Give the position of every Plasmodium parasite visible.
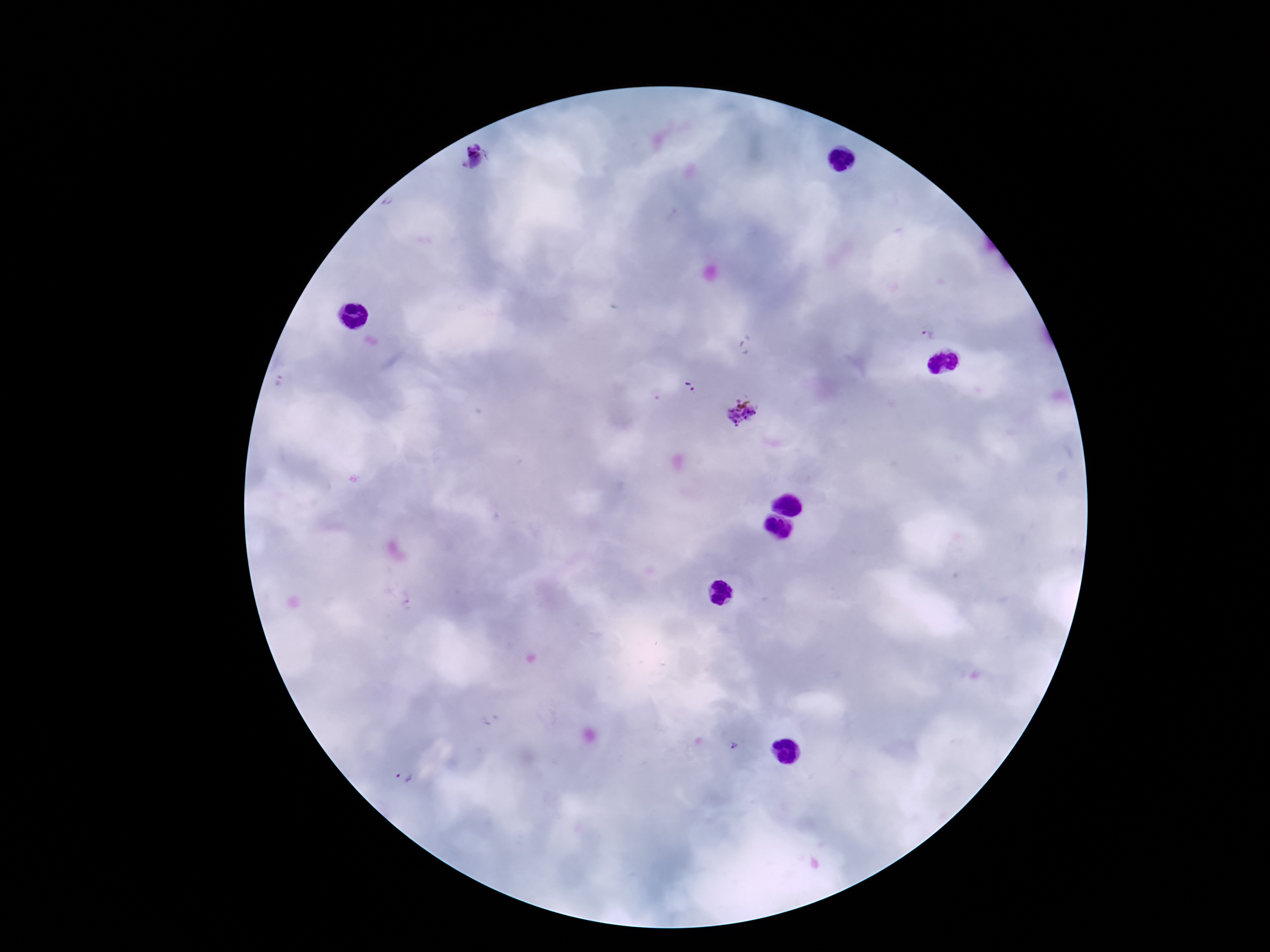
Approximate centers as [x, y] in pixels.
Plasmodium parasites: [473, 160], [926, 335], [691, 388], [743, 413], [733, 747], [404, 777].

preparation: thick blood film
stain: Giemsa
patient_malaria_status: infected
capture: smartphone camera through the microscope eyepiece
image_size: 1270×952 pixels
field_of_view: one from this slide
magnification: 100x